State which parasite is depicted.
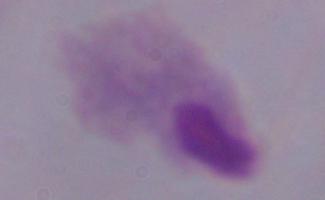

A trichomonad.

modality = photomicrograph
magnification = 1000x